Locate and identify every blood parasite.
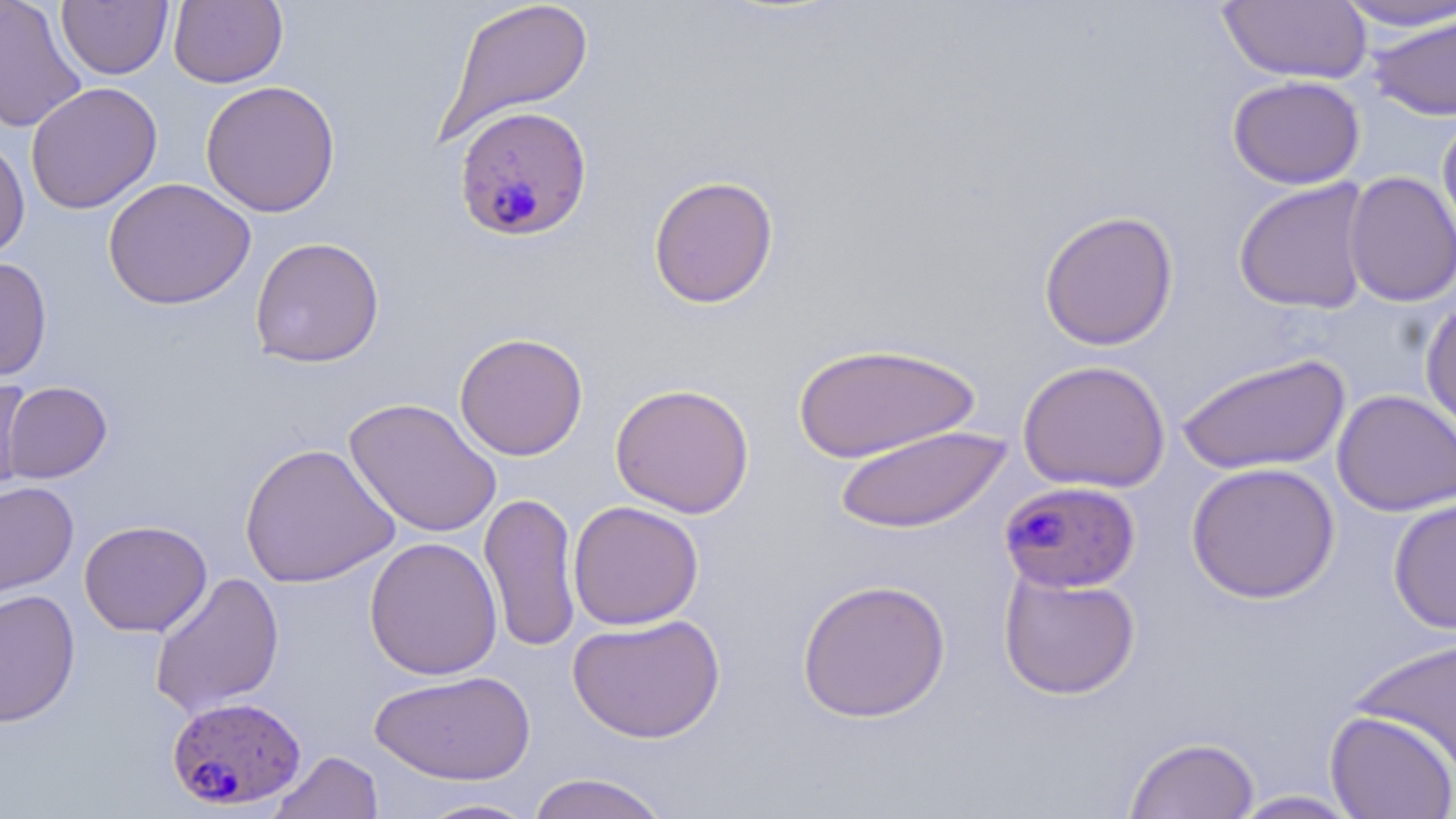
Approximate bounding boxes as (x1,y1)-(x2,y2) corner pairs in pixels.
Plasmodium falciparum-infected red blood cells: (453,105)-(593,242), (999,479)-(1141,595), (166,695)-(307,811).
No Plasmodium ovale, Plasmodium malariae, Plasmodium vivax, Babesia divergens, or Trypanosoma brucei observed.

Summary:
  - Uninfected red blood cell locations: (0,0)-(87,134), (57,0)-(173,80), (169,0)-(288,88), (436,0)-(594,143), (1217,0)-(1372,84), (1334,1)-(1456,32), (1367,10)-(1456,121), (1227,74)-(1365,189), (200,80)-(341,217), (25,81)-(162,215), (1437,114)-(1456,251), (0,136)-(30,260), (1343,171)-(1456,307), (648,174)-(779,309), (102,177)-(256,310), (1233,178)-(1373,314), (1038,209)-(1179,350), (249,236)-(385,368), (0,257)-(53,382), (1420,298)-(1456,437), (454,332)-(589,461), (791,342)-(981,463), (1176,352)-(1351,475), (1018,359)-(1171,493), (0,375)-(33,499), (3,381)-(112,483), (610,383)-(755,518), (1331,389)-(1456,517), (343,397)-(502,539), (835,425)-(1011,534), (239,442)-(399,588), (1185,461)-(1340,604), (0,481)-(79,600), (479,490)-(582,654), (1388,496)-(1456,634), (567,500)-(705,630), (78,519)-(212,637), (364,536)-(503,680), (149,571)-(285,718), (998,571)-(1141,700), (796,578)-(951,722), (0,588)-(80,726), (567,613)-(725,743), (1349,637)-(1456,772), (368,669)-(536,786), (1324,709)-(1456,818), (1123,736)-(1260,819), (268,750)-(383,819), (526,772)-(672,819), (1226,790)-(1364,818), (410,797)-(542,818)
  - Slide-level diagnosis: Plasmodium falciparum
  - Stain: May-Grünwald-Giemsa
  - Preparation: thin blood smear
  - Magnification: 1000x
  - Field of view: one of a larger specimen
  - Image size: 1456×819 pixels
  - Modality: light microscopy